Identify the blood parasite species.
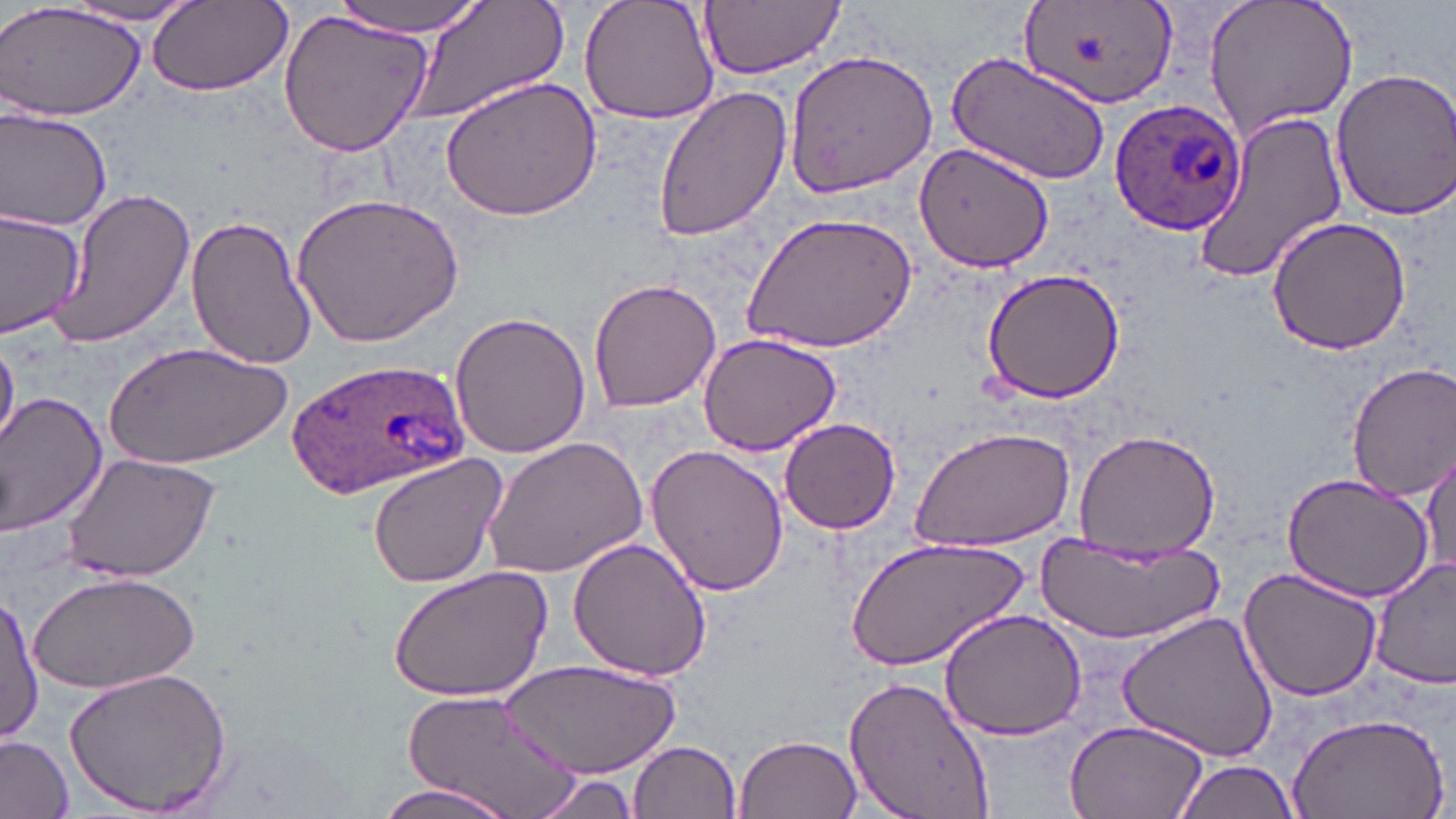
Plasmodium ovale.

Summary:
  - Coordinate format: approximate bounding boxes as named x1/y1/x2/y2 corners in pixels
  - Plasmodium ovale-infected red blood cell locations: (x1=1109, y1=100, x2=1245, y2=239), (x1=283, y1=355, x2=472, y2=498)
  - Uninfected red blood cell locations: (x1=0, y1=0, x2=147, y2=121), (x1=335, y1=0, x2=487, y2=34), (x1=404, y1=0, x2=569, y2=123), (x1=578, y1=0, x2=723, y2=124), (x1=699, y1=0, x2=844, y2=79), (x1=1202, y1=0, x2=1359, y2=141), (x1=148, y1=1, x2=293, y2=98), (x1=1016, y1=1, x2=1181, y2=113), (x1=61, y1=2, x2=206, y2=27), (x1=279, y1=8, x2=434, y2=160), (x1=784, y1=49, x2=939, y2=197), (x1=944, y1=51, x2=1112, y2=185), (x1=1327, y1=65, x2=1456, y2=222), (x1=439, y1=73, x2=603, y2=222), (x1=652, y1=82, x2=793, y2=242), (x1=0, y1=105, x2=113, y2=233), (x1=1190, y1=110, x2=1349, y2=285), (x1=918, y1=141, x2=1058, y2=272), (x1=45, y1=188, x2=197, y2=349), (x1=291, y1=189, x2=463, y2=347), (x1=0, y1=207, x2=86, y2=337), (x1=741, y1=213, x2=916, y2=356), (x1=185, y1=214, x2=315, y2=369), (x1=1266, y1=215, x2=1412, y2=358), (x1=979, y1=269, x2=1126, y2=405), (x1=587, y1=277, x2=721, y2=413), (x1=449, y1=308, x2=590, y2=459), (x1=696, y1=332, x2=843, y2=459), (x1=0, y1=338, x2=19, y2=453), (x1=105, y1=339, x2=293, y2=467), (x1=1345, y1=362, x2=1456, y2=501), (x1=0, y1=391, x2=108, y2=537), (x1=778, y1=418, x2=903, y2=535), (x1=910, y1=427, x2=1077, y2=554), (x1=1072, y1=428, x2=1221, y2=556), (x1=480, y1=436, x2=645, y2=580), (x1=1422, y1=444, x2=1454, y2=582), (x1=644, y1=445, x2=790, y2=598), (x1=61, y1=451, x2=220, y2=585), (x1=365, y1=454, x2=508, y2=590), (x1=1280, y1=474, x2=1433, y2=605), (x1=850, y1=534, x2=1027, y2=672), (x1=1033, y1=535, x2=1224, y2=641), (x1=568, y1=537, x2=714, y2=683), (x1=1371, y1=560, x2=1455, y2=690), (x1=387, y1=565, x2=553, y2=703), (x1=1238, y1=566, x2=1383, y2=702), (x1=31, y1=569, x2=201, y2=695), (x1=1, y1=591, x2=41, y2=748), (x1=938, y1=606, x2=1089, y2=740), (x1=1118, y1=609, x2=1279, y2=764), (x1=500, y1=660, x2=679, y2=777), (x1=60, y1=666, x2=236, y2=817), (x1=843, y1=674, x2=999, y2=819), (x1=397, y1=687, x2=588, y2=817), (x1=1286, y1=707, x2=1450, y2=819), (x1=1061, y1=716, x2=1211, y2=819), (x1=735, y1=732, x2=862, y2=819), (x1=0, y1=734, x2=74, y2=818), (x1=630, y1=740, x2=743, y2=819), (x1=1172, y1=757, x2=1301, y2=819), (x1=529, y1=769, x2=649, y2=819), (x1=368, y1=779, x2=521, y2=819)
  - Modality: light microscopy
  - Magnification: 1000x
  - Stain: May-Grünwald-Giemsa
  - Field of view: single
  - Image size: 1456×819 pixels
  - Preparation: thin blood film